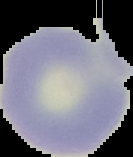
{
  "result": "no Plasmodium parasites detected",
  "preparation": "thin blood smear",
  "image_size": "133×157 pixels",
  "image_type": "cell region segmented out of the field of view; surrounding area masked to black"
}